Assess for malaria.
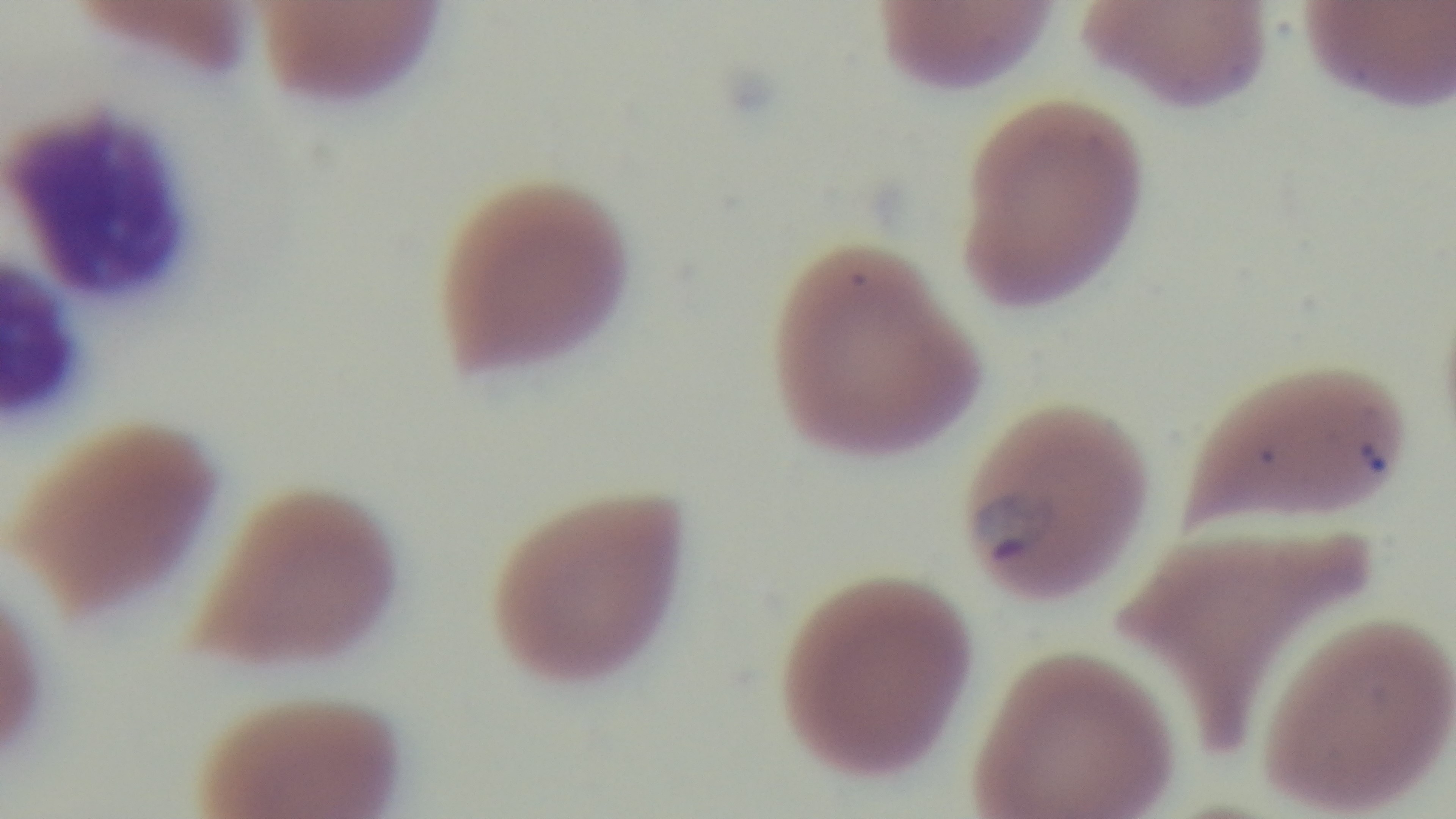
It is infected.

preparation = thin blood film
capture = mounted 4K digital camera
stain = Giemsa
field of view = single
modality = light microscopy
objective = 100x oil immersion